State which parasite is depicted.
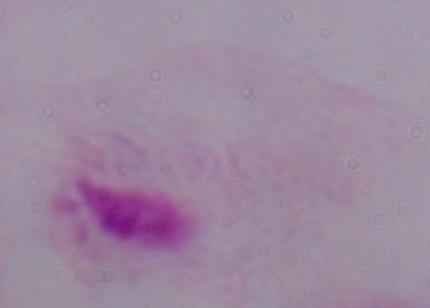
A trichomonad.

Micrograph. Captured at 1000x magnification.